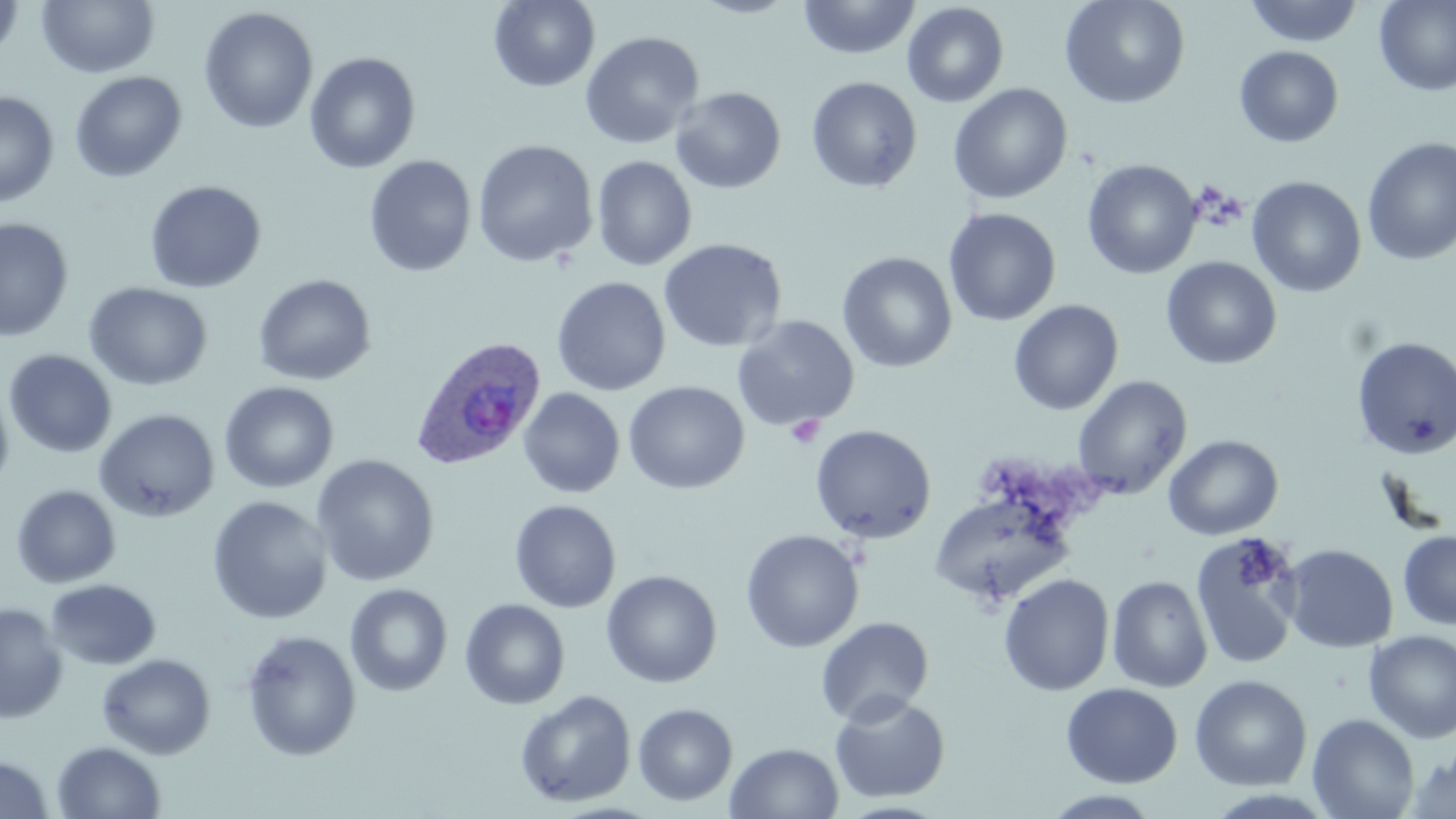
slide-level diagnosis = Plasmodium ovale
field of view = single
uninfected red blood cell locations = approximate bounding boxes as named x1/y1/x2/y2 corners in pixels: (x1=0, y1=0, x2=25, y2=60), (x1=488, y1=0, x2=600, y2=92), (x1=688, y1=0, x2=802, y2=18), (x1=798, y1=0, x2=920, y2=60), (x1=1059, y1=0, x2=1191, y2=109), (x1=1244, y1=0, x2=1365, y2=47), (x1=37, y1=1, x2=160, y2=79), (x1=1373, y1=1, x2=1456, y2=96), (x1=902, y1=2, x2=1009, y2=108), (x1=198, y1=7, x2=319, y2=134), (x1=579, y1=31, x2=704, y2=149), (x1=1234, y1=46, x2=1344, y2=147), (x1=304, y1=51, x2=421, y2=174), (x1=69, y1=71, x2=188, y2=183), (x1=806, y1=76, x2=922, y2=193), (x1=948, y1=83, x2=1073, y2=205), (x1=670, y1=87, x2=786, y2=194), (x1=0, y1=91, x2=60, y2=207), (x1=1361, y1=137, x2=1456, y2=267), (x1=472, y1=140, x2=598, y2=268), (x1=364, y1=155, x2=477, y2=277), (x1=591, y1=155, x2=697, y2=271), (x1=1082, y1=159, x2=1201, y2=280), (x1=1246, y1=176, x2=1367, y2=298), (x1=144, y1=180, x2=267, y2=293), (x1=943, y1=207, x2=1061, y2=327), (x1=0, y1=217, x2=74, y2=342), (x1=658, y1=238, x2=787, y2=354), (x1=837, y1=252, x2=957, y2=372), (x1=1161, y1=256, x2=1282, y2=370), (x1=252, y1=274, x2=377, y2=386), (x1=551, y1=277, x2=670, y2=396), (x1=84, y1=282, x2=213, y2=391), (x1=1008, y1=299, x2=1124, y2=416), (x1=732, y1=315, x2=860, y2=432), (x1=1351, y1=335, x2=1456, y2=459), (x1=3, y1=349, x2=118, y2=458), (x1=1071, y1=375, x2=1192, y2=499), (x1=218, y1=381, x2=339, y2=493), (x1=623, y1=381, x2=749, y2=495), (x1=0, y1=382, x2=15, y2=497), (x1=518, y1=388, x2=624, y2=499), (x1=94, y1=408, x2=220, y2=523), (x1=810, y1=424, x2=937, y2=544), (x1=1163, y1=434, x2=1284, y2=540), (x1=311, y1=454, x2=440, y2=587), (x1=11, y1=484, x2=121, y2=589), (x1=928, y1=491, x2=1077, y2=610), (x1=207, y1=496, x2=333, y2=625), (x1=509, y1=500, x2=621, y2=613), (x1=740, y1=529, x2=864, y2=653), (x1=1398, y1=529, x2=1456, y2=630), (x1=1191, y1=533, x2=1304, y2=670), (x1=1282, y1=544, x2=1398, y2=653), (x1=601, y1=570, x2=722, y2=688), (x1=998, y1=574, x2=1114, y2=696), (x1=1106, y1=575, x2=1213, y2=693), (x1=45, y1=579, x2=161, y2=670), (x1=344, y1=583, x2=453, y2=697), (x1=459, y1=598, x2=570, y2=710), (x1=0, y1=602, x2=68, y2=723), (x1=815, y1=616, x2=934, y2=726), (x1=240, y1=629, x2=362, y2=762), (x1=1364, y1=629, x2=1456, y2=743), (x1=97, y1=653, x2=217, y2=759), (x1=1189, y1=675, x2=1312, y2=791), (x1=1061, y1=682, x2=1183, y2=788), (x1=515, y1=689, x2=637, y2=808), (x1=829, y1=693, x2=951, y2=803), (x1=632, y1=703, x2=738, y2=806), (x1=1307, y1=713, x2=1420, y2=819), (x1=52, y1=741, x2=166, y2=819), (x1=725, y1=742, x2=844, y2=819), (x1=1404, y1=747, x2=1456, y2=818), (x1=0, y1=755, x2=55, y2=819), (x1=1042, y1=790, x2=1164, y2=818)
stain = May-Grünwald-Giemsa
Plasmodium ovale-infected red blood cell locations = approximate bounding boxes as named x1/y1/x2/y2 corners in pixels: (x1=410, y1=335, x2=546, y2=470)
platelet locations = approximate bounding boxes as named x1/y1/x2/y2 corners in pixels: (x1=785, y1=415, x2=825, y2=449), (x1=1231, y1=538, x2=1284, y2=591)
image size = 1456×819 pixels
magnification = 1000x
preparation = thin blood smear
modality = light microscopy